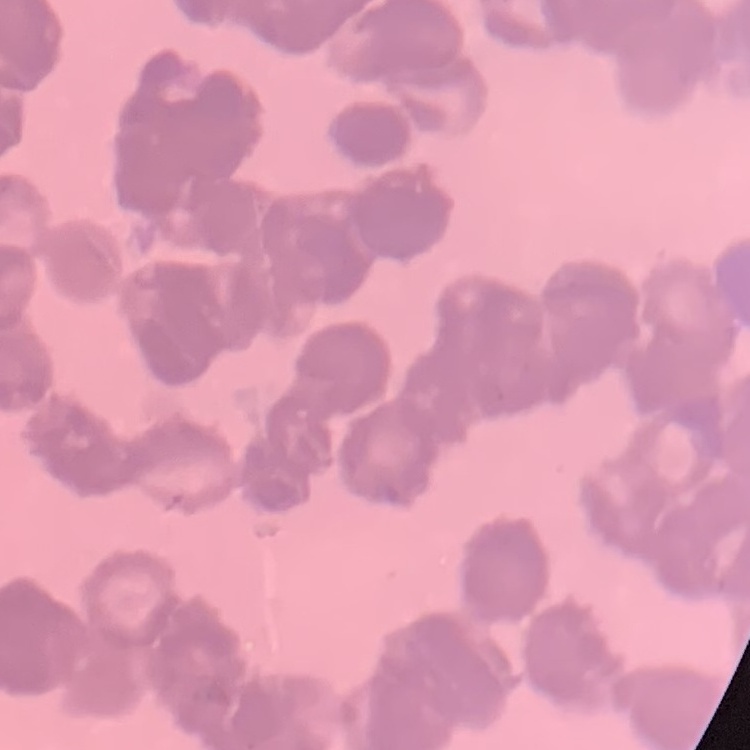

Summary:
  - Erythrocyte morphology: rouleaux formation
  - Stain: Field's or Giemsa
  - Preparation: thin peripheral smear
  - Image type: square crop of a larger photomicrograph